Report the malaria status of this cell.
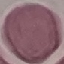
Uninfected.

Acquired by smartphone through the microscope eyepiece. Thin blood smear. Giemsa-stained preparation. Cell patch, automatically extracted from a larger field of view and resized to 64 × 64 pixels.